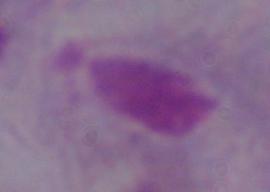
A trichomonad is shown. Captured at 1000x magnification. Micrograph.